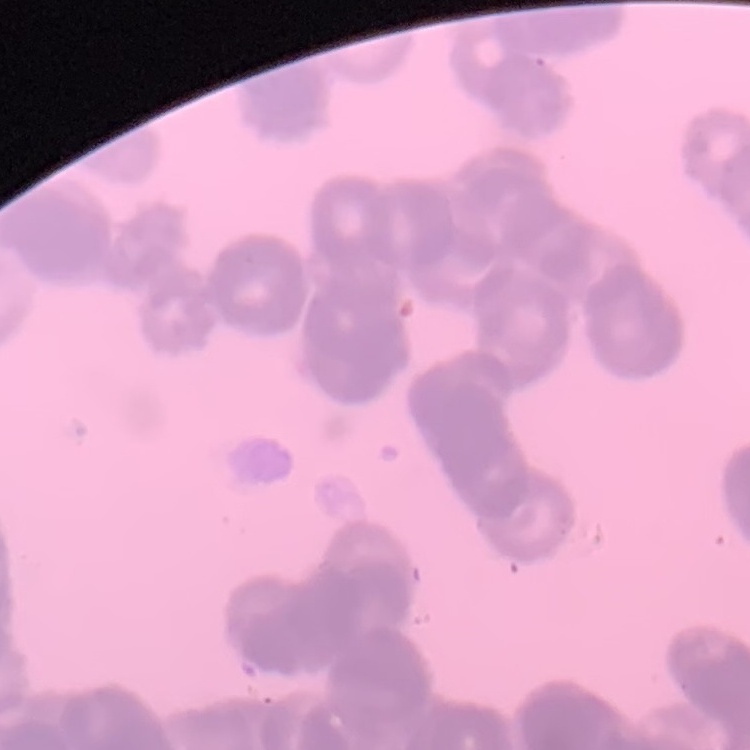

The red blood cells show rouleaux formation. Thin blood film. One tile cut from a larger photomicrograph. Field's or Giemsa stain.